State which parasite is depicted.
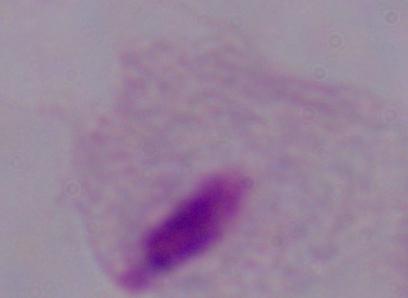

This is a trichomonad.

Photomicrograph. 1000x magnification.